Locate and identify every blood parasite.
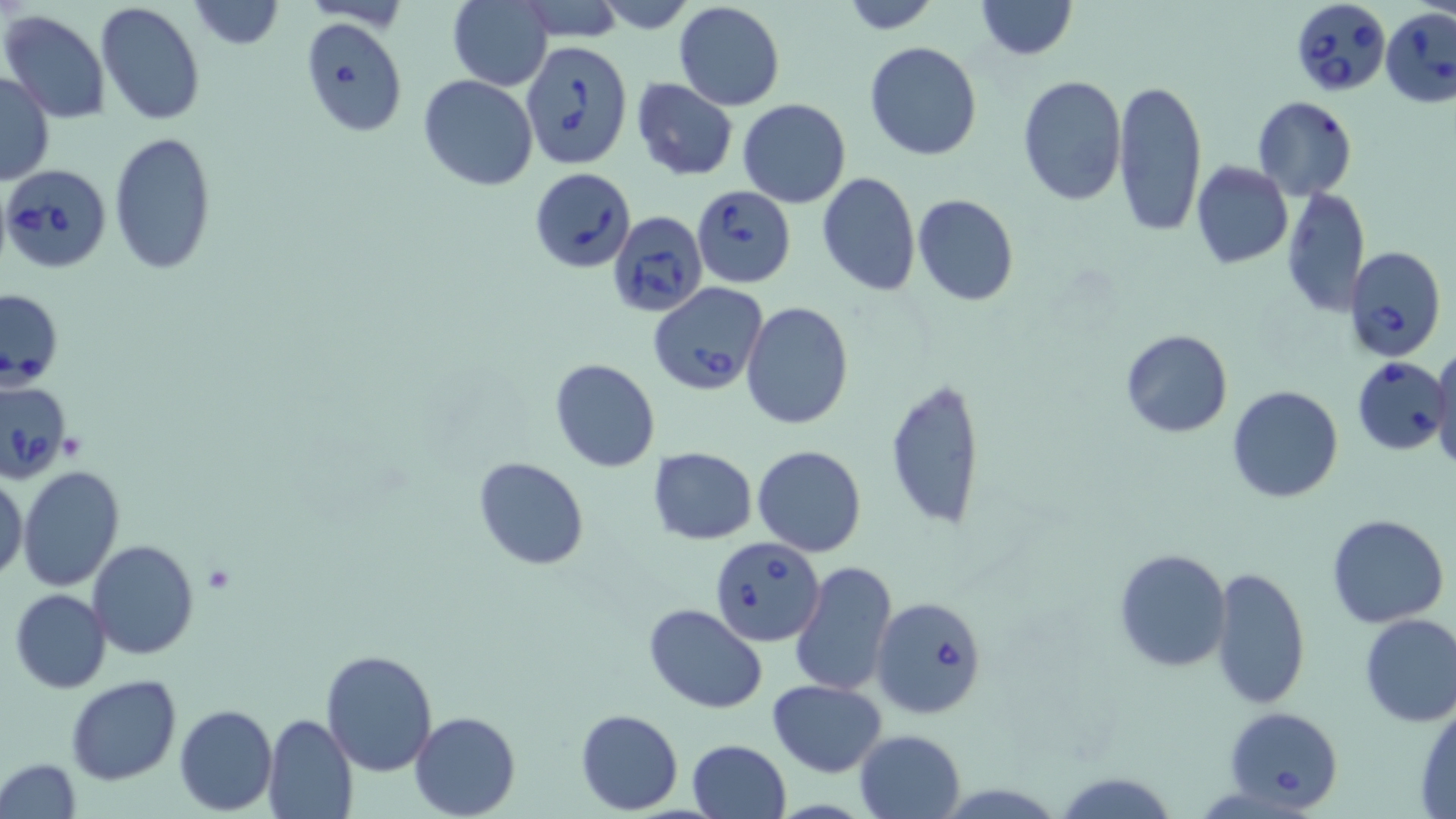

Approximate bounding boxes as (x1,y1)-(x2,y2) corner pairs in pixels.
Babesia divergens-infected red blood cells: (1290,3)-(1395,99), (1380,4)-(1456,112), (300,17)-(408,138), (519,40)-(635,176), (0,163)-(104,273), (529,167)-(636,272), (692,186)-(796,287), (608,211)-(708,315), (1344,245)-(1446,360), (649,282)-(769,395), (1,290)-(62,385), (1353,357)-(1451,455), (0,379)-(72,482), (710,536)-(825,647), (870,595)-(988,717), (1223,706)-(1344,813).
No Plasmodium falciparum, Plasmodium ovale, Plasmodium malariae, Plasmodium vivax, or Trypanosoma brucei observed.

Platelet locations: (204,563)-(237,592). Uninfected red blood cell locations: (186,0)-(284,49), (974,0)-(1076,59), (447,1)-(553,90), (837,1)-(946,32), (95,2)-(206,127), (675,3)-(785,110), (1,10)-(111,122), (863,40)-(984,161), (0,72)-(52,185), (420,75)-(537,190), (1015,75)-(1127,208), (1112,77)-(1208,239), (631,78)-(738,181), (1251,97)-(1357,200), (738,98)-(851,207), (108,131)-(217,275), (1191,161)-(1293,268), (815,172)-(921,296), (1282,187)-(1369,317), (913,194)-(1019,307), (740,300)-(853,432), (1120,328)-(1233,438), (1431,343)-(1456,474), (549,358)-(661,472), (885,378)-(988,530), (1226,384)-(1344,503), (752,444)-(866,557), (648,448)-(758,544), (473,456)-(592,571), (18,464)-(125,591), (0,475)-(27,584), (1325,513)-(1449,627), (88,539)-(198,659), (1113,547)-(1231,673), (789,561)-(898,697), (1211,565)-(1310,707), (9,589)-(113,693), (644,604)-(766,713), (1358,613)-(1456,727), (320,647)-(438,777), (66,674)-(181,786), (769,679)-(888,777), (1413,698)-(1456,815), (174,704)-(276,814), (576,709)-(683,813), (409,710)-(520,819), (263,712)-(357,819), (851,728)-(964,817), (686,739)-(792,819), (0,758)-(81,818). Slide-level diagnosis: Babesia divergens. Light microscopy. One field of a larger specimen. May-Grünwald-Giemsa-stained preparation. Thin blood smear. Image is 1456×819 pixels. 1000x magnification.